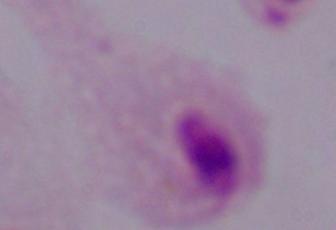
magnification = 1000x
modality = photomicrograph
identification = trichomonad